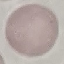 Result: no malaria parasites seen. Cell patch, automatically extracted from a larger field of view and resized to 64 × 64 pixels. Giemsa-stained preparation. Photographed with a smartphone camera at the microscope eyepiece. Thin blood film.